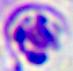
Summary:
  - Modality: micrograph
  - Magnification: 400x
  - Identification: leukocyte